Outline each blood parasite and name the species.
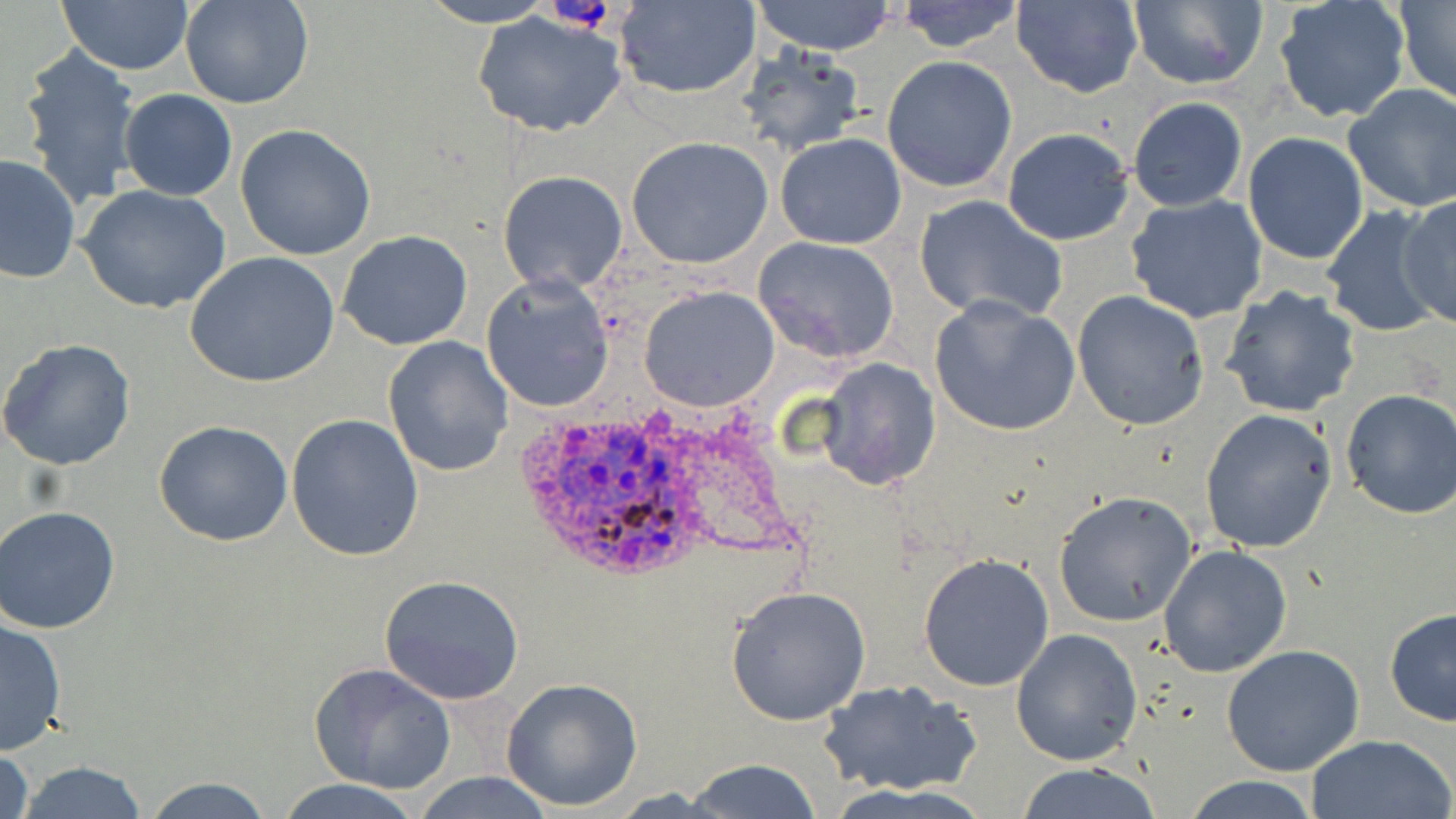

Approximate bounding boxes as named x1/y1/x2/y2 corners in pixels.
Plasmodium ovale-infected red blood cells: (x1=518, y1=411, x2=707, y2=585).
No Plasmodium falciparum, Plasmodium malariae, Plasmodium vivax, Babesia divergens, or Trypanosoma brucei observed.

Platelet locations: (x1=546, y1=0, x2=617, y2=30). Uninfected red blood cell locations: (x1=58, y1=0, x2=195, y2=74), (x1=180, y1=0, x2=314, y2=109), (x1=416, y1=0, x2=558, y2=27), (x1=611, y1=0, x2=762, y2=100), (x1=748, y1=0, x2=899, y2=55), (x1=892, y1=0, x2=1028, y2=54), (x1=1273, y1=0, x2=1411, y2=125), (x1=1012, y1=1, x2=1144, y2=98), (x1=1124, y1=1, x2=1268, y2=90), (x1=1397, y1=1, x2=1456, y2=102), (x1=472, y1=10, x2=628, y2=138), (x1=733, y1=43, x2=865, y2=158), (x1=18, y1=45, x2=144, y2=214), (x1=882, y1=55, x2=1018, y2=193), (x1=1342, y1=83, x2=1456, y2=211), (x1=118, y1=89, x2=237, y2=201), (x1=1126, y1=97, x2=1249, y2=211), (x1=1006, y1=113, x2=1249, y2=229), (x1=235, y1=125, x2=375, y2=260), (x1=1001, y1=127, x2=1135, y2=245), (x1=775, y1=131, x2=908, y2=250), (x1=1242, y1=132, x2=1369, y2=265), (x1=626, y1=137, x2=774, y2=269), (x1=0, y1=152, x2=80, y2=287), (x1=498, y1=169, x2=628, y2=294), (x1=79, y1=185, x2=231, y2=316), (x1=1125, y1=193, x2=1269, y2=323), (x1=913, y1=194, x2=1068, y2=323), (x1=1395, y1=194, x2=1456, y2=329), (x1=1320, y1=204, x2=1444, y2=338), (x1=336, y1=231, x2=475, y2=351), (x1=752, y1=236, x2=900, y2=362), (x1=187, y1=252, x2=341, y2=391), (x1=482, y1=272, x2=614, y2=413), (x1=639, y1=285, x2=781, y2=412), (x1=1220, y1=286, x2=1361, y2=417), (x1=1072, y1=289, x2=1209, y2=431), (x1=929, y1=295, x2=1082, y2=436), (x1=382, y1=336, x2=514, y2=478), (x1=0, y1=338, x2=136, y2=470), (x1=816, y1=358, x2=941, y2=490), (x1=1337, y1=387, x2=1456, y2=520), (x1=1199, y1=409, x2=1338, y2=554), (x1=286, y1=414, x2=424, y2=562), (x1=155, y1=419, x2=294, y2=546), (x1=1053, y1=493, x2=1196, y2=626), (x1=0, y1=505, x2=121, y2=634), (x1=1158, y1=546, x2=1293, y2=679), (x1=918, y1=552, x2=1054, y2=692), (x1=378, y1=574, x2=525, y2=705), (x1=726, y1=585, x2=872, y2=727), (x1=1383, y1=608, x2=1455, y2=728), (x1=0, y1=616, x2=68, y2=754), (x1=1010, y1=628, x2=1143, y2=766), (x1=1219, y1=644, x2=1366, y2=777), (x1=310, y1=663, x2=456, y2=794), (x1=500, y1=676, x2=645, y2=812), (x1=817, y1=679, x2=983, y2=798), (x1=1301, y1=733, x2=1454, y2=819), (x1=0, y1=746, x2=35, y2=819), (x1=680, y1=759, x2=828, y2=818), (x1=14, y1=761, x2=151, y2=818), (x1=1012, y1=763, x2=1165, y2=819), (x1=412, y1=771, x2=556, y2=818), (x1=138, y1=774, x2=277, y2=818), (x1=1180, y1=775, x2=1323, y2=818), (x1=274, y1=777, x2=425, y2=819). Slide-level diagnosis: Plasmodium ovale. Thin blood smear. Optical microscopy. One field of a larger specimen. May-Grünwald-Giemsa-stained preparation. Image is 1456×819 pixels. 1000x magnification.